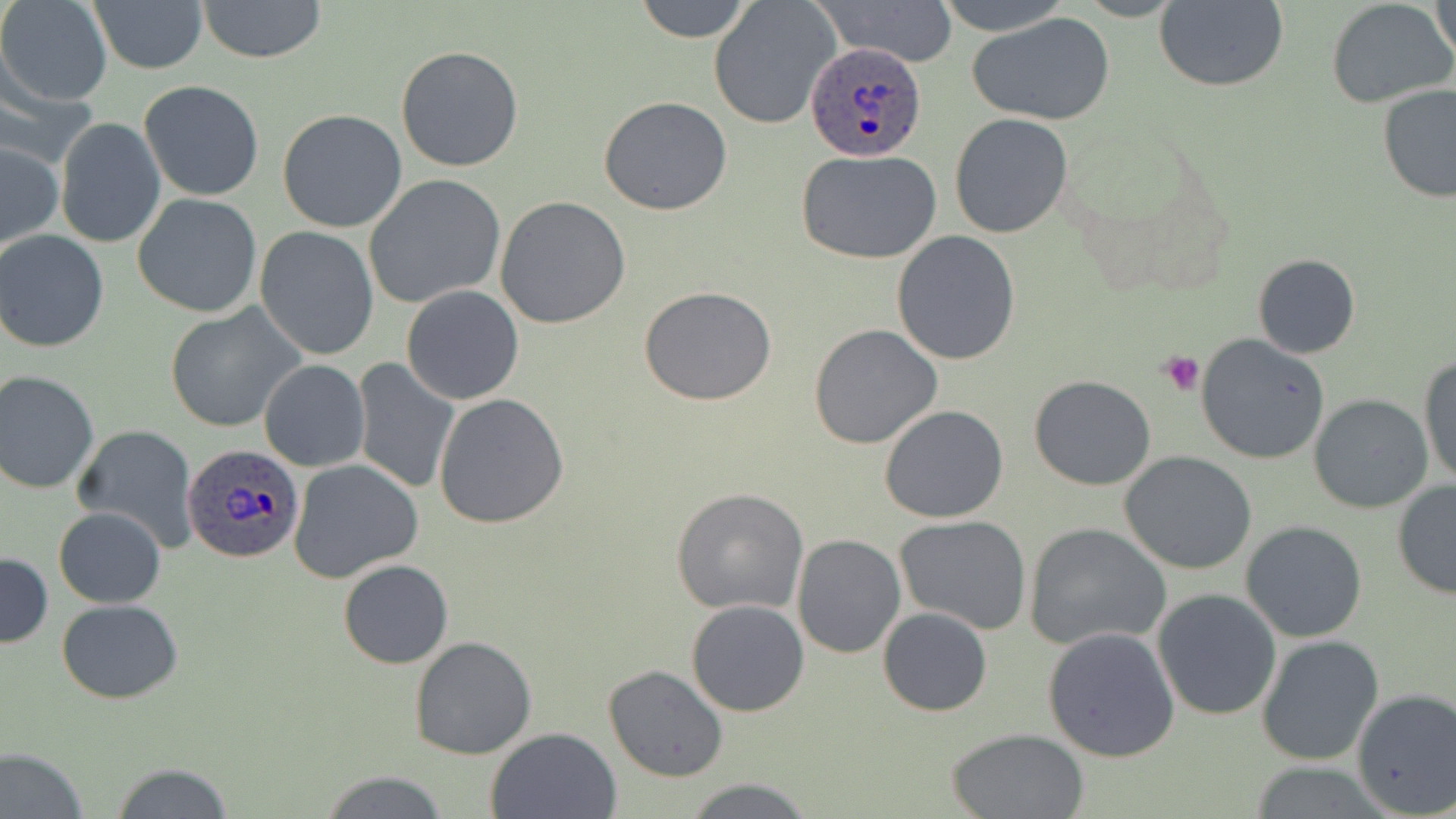
Approximate bounding boxes as named x1/y1/x2/y2 corners in pixels. Platelet locations: (x1=1161, y1=348, x2=1208, y2=396). Uninfected red blood cell locations: (x1=1, y1=0, x2=112, y2=106), (x1=86, y1=0, x2=209, y2=74), (x1=194, y1=0, x2=330, y2=64), (x1=633, y1=0, x2=755, y2=42), (x1=821, y1=0, x2=959, y2=68), (x1=932, y1=0, x2=1077, y2=36), (x1=1428, y1=0, x2=1456, y2=63), (x1=1154, y1=1, x2=1289, y2=92), (x1=1326, y1=1, x2=1455, y2=109), (x1=708, y1=2, x2=840, y2=130), (x1=969, y1=13, x2=1116, y2=126), (x1=395, y1=45, x2=525, y2=173), (x1=139, y1=80, x2=265, y2=201), (x1=1378, y1=84, x2=1456, y2=203), (x1=598, y1=96, x2=733, y2=217), (x1=277, y1=108, x2=407, y2=232), (x1=950, y1=114, x2=1074, y2=238), (x1=56, y1=116, x2=167, y2=250), (x1=0, y1=141, x2=63, y2=253), (x1=794, y1=149, x2=944, y2=263), (x1=364, y1=175, x2=506, y2=309), (x1=132, y1=193, x2=263, y2=318), (x1=494, y1=196, x2=630, y2=329), (x1=255, y1=226, x2=380, y2=361), (x1=0, y1=230, x2=112, y2=353), (x1=891, y1=230, x2=1022, y2=364), (x1=1252, y1=254, x2=1360, y2=359), (x1=401, y1=285, x2=524, y2=404), (x1=638, y1=285, x2=777, y2=405), (x1=164, y1=304, x2=304, y2=433), (x1=809, y1=324, x2=942, y2=450), (x1=1196, y1=334, x2=1331, y2=464), (x1=1420, y1=355, x2=1456, y2=486), (x1=259, y1=359, x2=369, y2=471), (x1=350, y1=360, x2=460, y2=493), (x1=0, y1=369, x2=100, y2=495), (x1=1029, y1=374, x2=1156, y2=490), (x1=434, y1=392, x2=569, y2=527), (x1=1309, y1=394, x2=1432, y2=513), (x1=879, y1=404, x2=1008, y2=523), (x1=71, y1=425, x2=199, y2=550), (x1=1120, y1=452, x2=1258, y2=574), (x1=289, y1=458, x2=423, y2=583), (x1=1391, y1=481, x2=1456, y2=599), (x1=670, y1=488, x2=808, y2=615), (x1=53, y1=507, x2=165, y2=609), (x1=895, y1=515, x2=1032, y2=635), (x1=1240, y1=520, x2=1368, y2=642), (x1=1024, y1=522, x2=1171, y2=652), (x1=791, y1=534, x2=907, y2=659), (x1=0, y1=552, x2=51, y2=647), (x1=338, y1=560, x2=453, y2=668), (x1=1152, y1=588, x2=1283, y2=721), (x1=57, y1=600, x2=184, y2=703), (x1=686, y1=600, x2=811, y2=717), (x1=877, y1=607, x2=992, y2=716), (x1=1043, y1=626, x2=1182, y2=761), (x1=1255, y1=634, x2=1386, y2=767), (x1=408, y1=636, x2=538, y2=759), (x1=603, y1=665, x2=728, y2=782), (x1=1351, y1=687, x2=1456, y2=818), (x1=486, y1=726, x2=624, y2=818), (x1=946, y1=727, x2=1088, y2=818), (x1=1, y1=746, x2=88, y2=819), (x1=108, y1=763, x2=234, y2=818), (x1=1242, y1=763, x2=1397, y2=817), (x1=321, y1=771, x2=449, y2=817), (x1=685, y1=778, x2=815, y2=817). Plasmodium ovale-infected red blood cell locations: (x1=802, y1=41, x2=928, y2=163), (x1=182, y1=444, x2=304, y2=566). Slide-level diagnosis: Plasmodium ovale. 1000x magnification. One field of a larger specimen. Thin blood film. Image is 1456×819 pixels. Light microscopy. May-Grünwald-Giemsa-stained preparation.